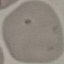

malaria status = uninfected
preparation = thin blood film
stain = Giemsa
capture = smartphone camera at the microscope eyepiece
image type = automatically extracted cell patch, resized to 64 × 64 pixels